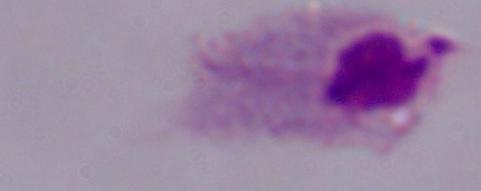
modality = micrograph
identification = trichomonad
magnification = 1000x